Look for parasitized red blood cells.
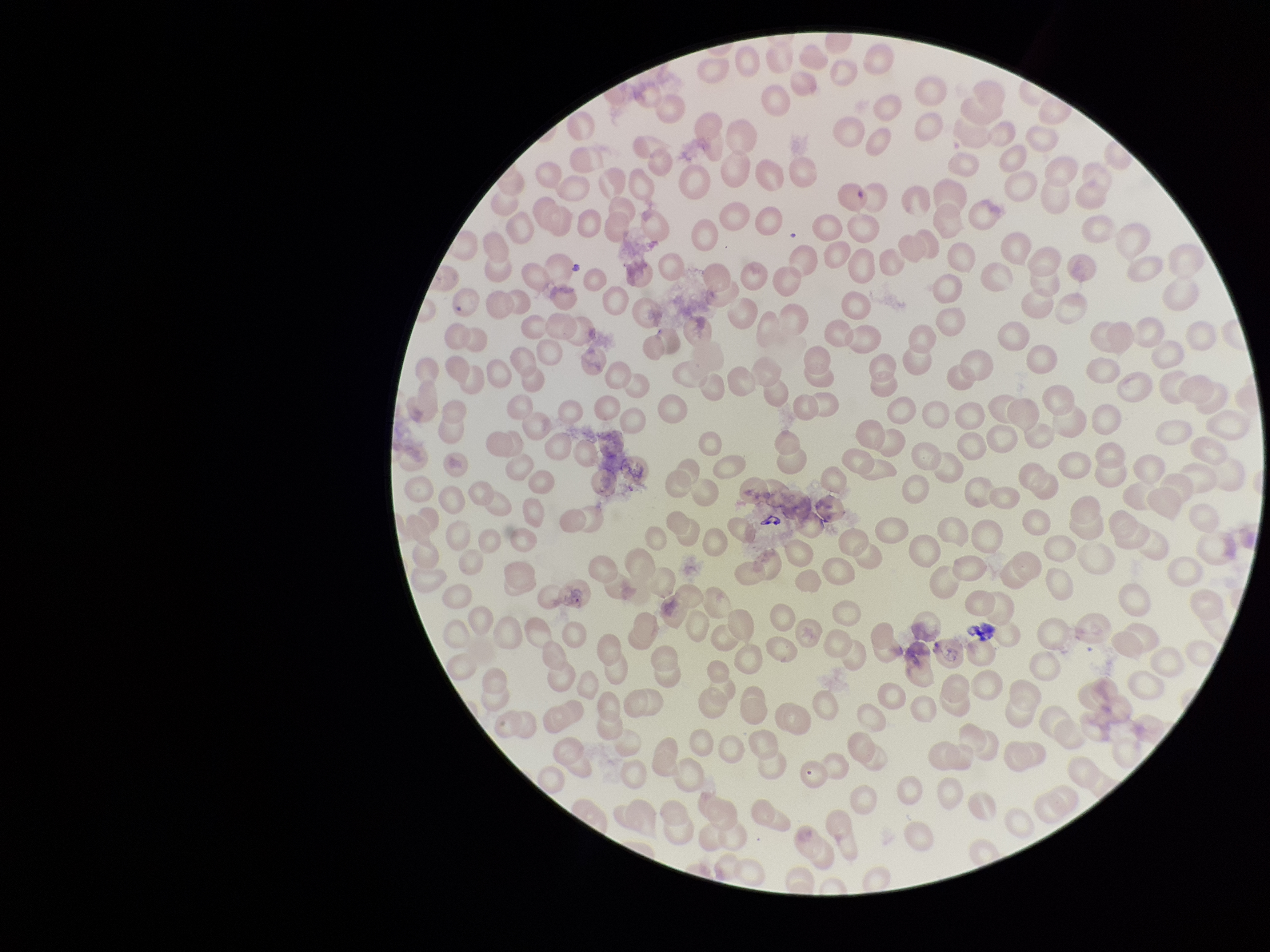
None identified.

Summary:
  - Parasitized red blood cell count: 0
  - Capture: smartphone photograph through the microscope eyepiece
  - Image size: 1270×952 pixels
  - Field of view: single
  - Red blood cell count: 267
  - Stain: Giemsa
  - Preparation: thin blood smear
  - Patient malaria status: negative